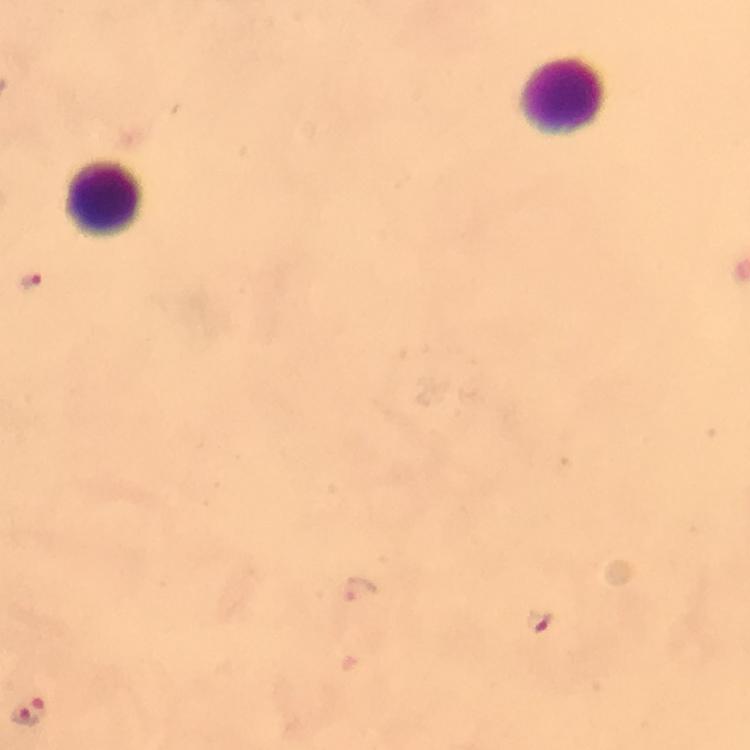
Approximate centers as [x, y] in pixels.
Summary:
  - Leukocyte locations: [565, 96], [104, 198]
  - Malaria parasite locations: [29, 281], [359, 589], [540, 621], [22, 717]
  - Cropped from: one field of view
  - Stain: Giemsa
  - Context: from a diagnostic examination for malaria
  - Image size: 750×750 pixels
  - Preparation: thick blood film
  - Immersion oil: used
  - Magnification: 100x
  - Capture: smartphone mounted on the microscope